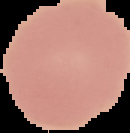
preparation = thin blood smear
image type = segmented cell region with the area outside set to black
image size = 130×133 pixels
result = no malaria parasites detected